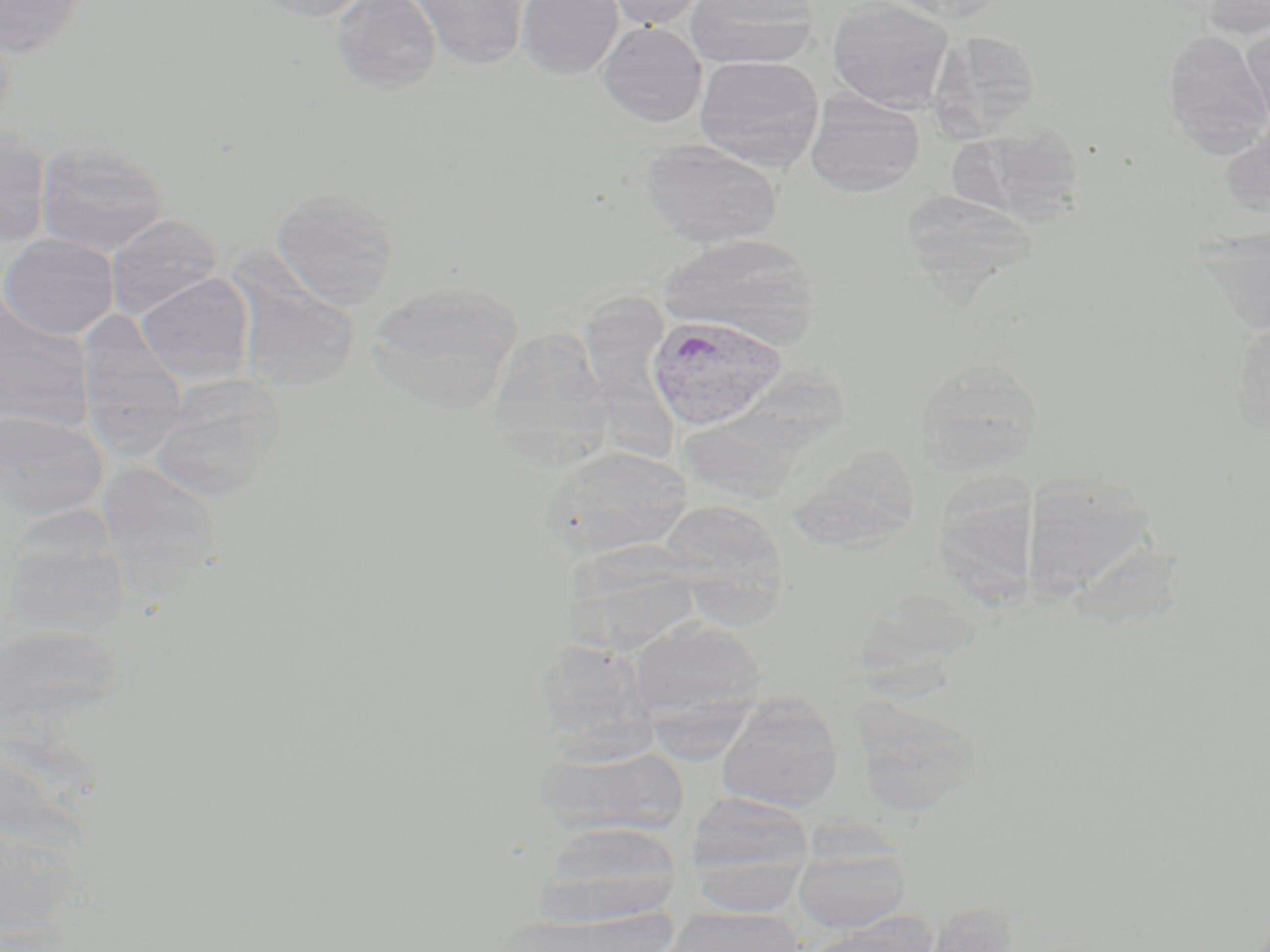

Summary:
  - Coordinate format: approximate bounding boxes as (x1, y1, x2, y2) in pixels
  - Plasmodium vivax-infected red blood cell locations: (646, 313, 786, 431)
  - Uninfected red blood cell locations: (0, 0, 85, 58), (257, 0, 375, 21), (332, 0, 442, 92), (412, 0, 529, 69), (516, 0, 623, 79), (606, 0, 708, 29), (685, 0, 819, 70), (827, 0, 955, 112), (878, 0, 1012, 24), (1199, 0, 1270, 39), (597, 22, 707, 127), (1240, 22, 1270, 132), (929, 30, 1042, 138), (1163, 31, 1270, 154), (694, 56, 825, 173), (805, 90, 925, 196), (1220, 121, 1270, 220), (955, 123, 1087, 224), (0, 126, 53, 248), (639, 138, 782, 248), (35, 142, 169, 257), (270, 188, 400, 309), (900, 189, 1038, 293), (106, 214, 222, 318), (0, 233, 120, 340), (659, 234, 820, 347), (135, 273, 255, 386), (232, 275, 360, 393), (365, 281, 523, 414), (587, 287, 673, 458), (0, 295, 96, 433), (76, 310, 187, 428), (1232, 317, 1270, 439), (487, 326, 613, 462), (913, 360, 1044, 476), (695, 375, 858, 499), (148, 382, 282, 503), (0, 410, 108, 521), (787, 443, 923, 550), (553, 446, 692, 555), (97, 464, 224, 582), (1020, 473, 1159, 601), (656, 499, 788, 609), (1, 537, 129, 639), (566, 543, 704, 655), (627, 618, 767, 727), (0, 621, 125, 748), (533, 638, 655, 754), (850, 695, 985, 816), (716, 696, 844, 813), (535, 745, 688, 838), (685, 793, 816, 912), (535, 820, 683, 927), (791, 840, 913, 935), (920, 903, 1021, 951), (663, 905, 805, 952), (797, 920, 936, 952)
  - Slide-level diagnosis: Plasmodium vivax
  - Image size: 1270×952 pixels
  - Preparation: thin blood film
  - Stain: May-Grünwald-Giemsa
  - Modality: light microscopy
  - Field of view: single
  - Magnification: 1000x